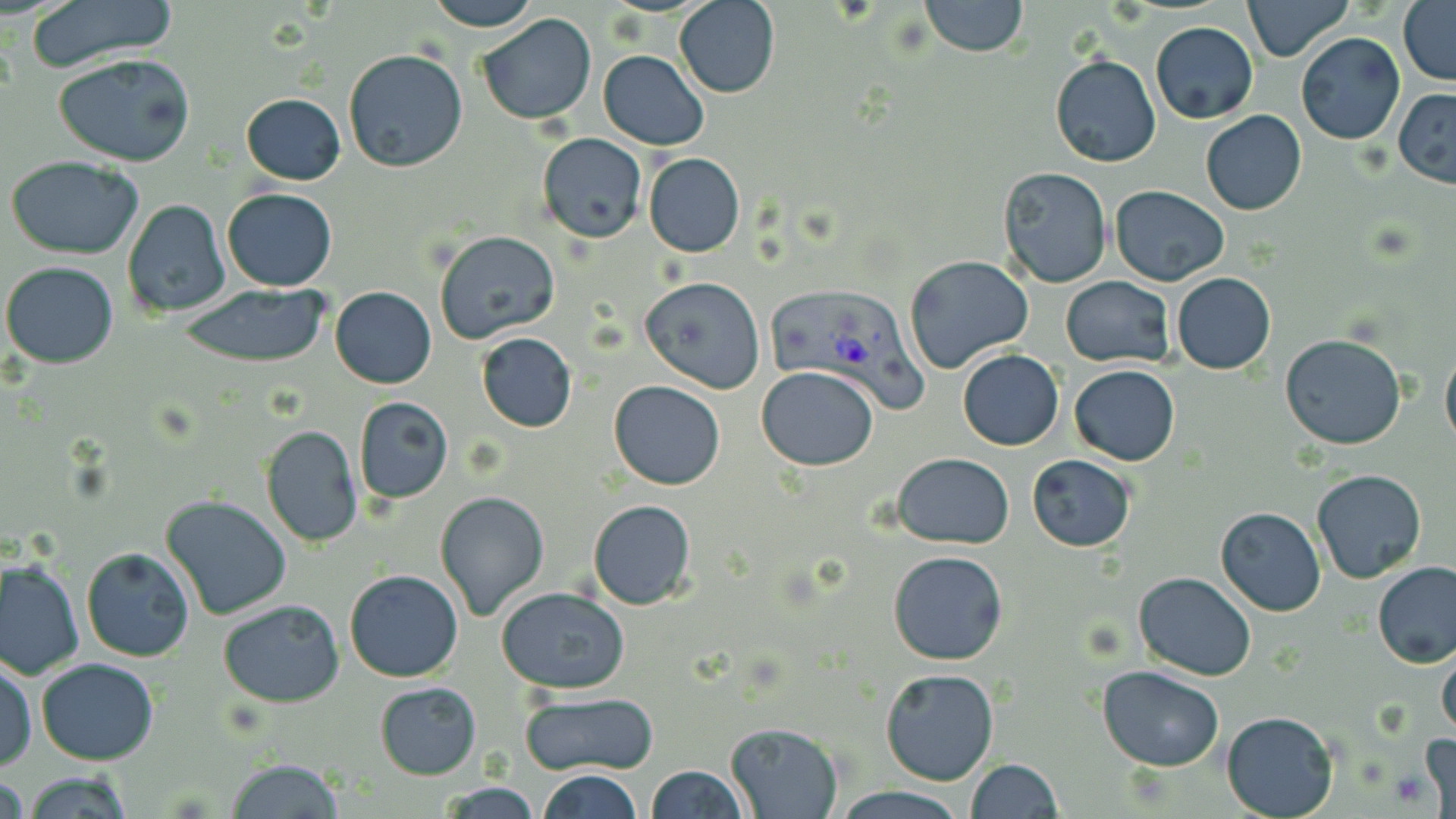
Plasmodium vivax-infected red blood cell locations = approximate bounding boxes as [x1, y1, x2, y2] in pixels: [768, 286, 928, 415]
slide-level diagnosis = Plasmodium vivax
stain = May-Grünwald-Giemsa
magnification = 1000x
preparation = thin blood smear
modality = optical microscopy
uninfected red blood cell locations = approximate bounding boxes as [x1, y1, x2, y2] in pixels: [23, 0, 179, 71], [421, 0, 543, 32], [674, 0, 780, 98], [918, 0, 1029, 57], [1241, 0, 1354, 64], [1399, 2, 1456, 83], [476, 12, 598, 127], [1150, 21, 1258, 125], [1296, 32, 1405, 145], [342, 48, 469, 175], [598, 49, 710, 151], [54, 51, 197, 167], [1051, 54, 1160, 167], [1393, 88, 1456, 189], [241, 92, 345, 185], [1201, 110, 1307, 216], [537, 133, 647, 242], [643, 153, 745, 256], [5, 155, 145, 259], [997, 165, 1113, 288], [1109, 184, 1230, 286], [223, 188, 337, 292], [122, 198, 230, 318], [434, 231, 560, 343], [904, 255, 1034, 374], [1, 261, 120, 368], [1172, 272, 1275, 374], [1060, 276, 1174, 368], [638, 277, 765, 393], [176, 284, 331, 369], [330, 286, 436, 388], [476, 333, 576, 432], [1279, 334, 1407, 450], [1441, 337, 1456, 451], [957, 349, 1064, 450], [1069, 364, 1180, 465], [757, 365, 880, 470], [609, 379, 725, 490], [353, 395, 453, 504], [262, 426, 363, 547], [892, 453, 1015, 549], [1027, 453, 1136, 551], [1312, 469, 1428, 584], [435, 491, 550, 620], [159, 495, 293, 621], [587, 499, 697, 610], [1215, 506, 1325, 615], [81, 546, 196, 662], [888, 550, 1008, 666], [1, 556, 83, 680], [1373, 563, 1456, 668], [344, 569, 464, 682], [1134, 571, 1256, 679], [497, 586, 631, 694], [217, 599, 345, 707], [1437, 647, 1456, 737], [1, 656, 36, 773], [37, 658, 158, 765], [1096, 665, 1225, 771], [880, 668, 999, 786], [374, 681, 482, 780], [519, 690, 659, 776], [1221, 709, 1340, 818], [724, 721, 843, 818], [1416, 734, 1455, 818], [967, 758, 1063, 818], [225, 759, 346, 818], [644, 765, 747, 819], [22, 770, 134, 817], [537, 770, 643, 818], [1, 773, 27, 819], [436, 782, 546, 817], [833, 785, 964, 819]
field of view = single
image size = 1456×819 pixels